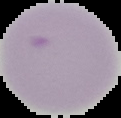
From a thin blood smear. Segmented cell region on a black background. Image is 121×118 pixels. Result: no Plasmodium parasites detected.